Report the malaria status of this cell.
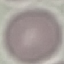
It is uninfected.

Summary:
  - Preparation: thin blood smear
  - Capture: smartphone camera at the microscope eyepiece
  - Stain: Giemsa
  - Image type: cell patch, automatically extracted from a larger field of view and resized to 64 × 64 pixels